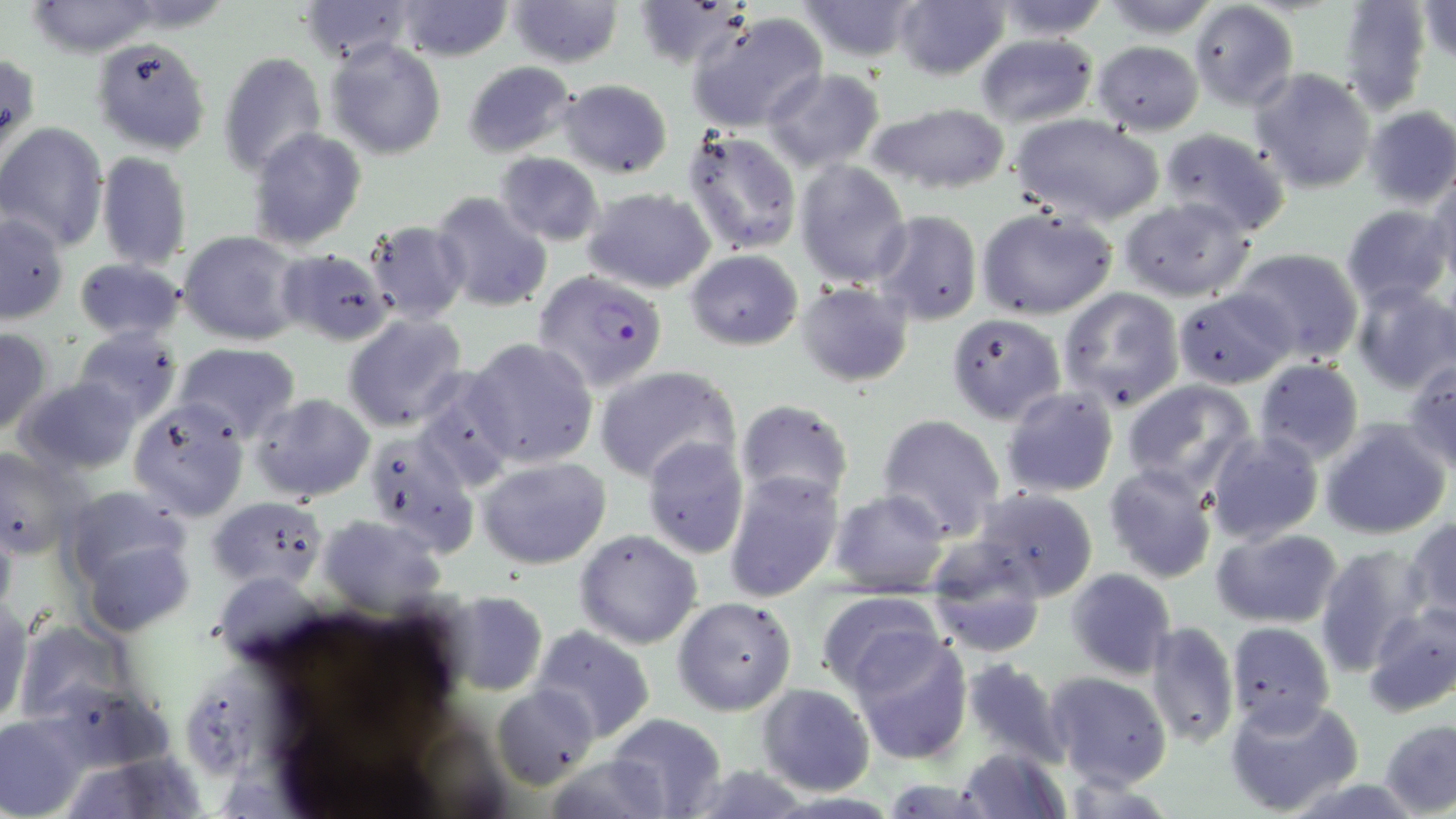
Approximate bounding boxes as [x1, y1, x2, y2] in pixels. Uninfected red blood cell locations: [22, 0, 169, 57], [396, 0, 513, 61], [507, 0, 625, 68], [792, 0, 925, 62], [893, 0, 1010, 81], [984, 0, 1113, 39], [1096, 0, 1224, 37], [1418, 0, 1455, 64], [295, 1, 419, 65], [1337, 1, 1433, 114], [1190, 2, 1298, 113], [686, 13, 827, 134], [975, 34, 1097, 126], [90, 36, 212, 156], [323, 38, 448, 160], [1092, 40, 1204, 133], [217, 51, 327, 176], [461, 60, 579, 159], [761, 68, 886, 172], [1250, 69, 1378, 194], [555, 79, 674, 179], [861, 103, 1012, 197], [1364, 105, 1456, 210], [1008, 114, 1166, 226], [0, 122, 108, 249], [247, 128, 368, 250], [682, 128, 801, 256], [1159, 128, 1291, 238], [95, 151, 193, 270], [494, 151, 606, 246], [794, 160, 911, 287], [1427, 174, 1456, 288], [581, 186, 715, 293], [430, 192, 554, 313], [1118, 197, 1257, 302], [1340, 205, 1451, 309], [975, 206, 1120, 320], [871, 209, 982, 325], [0, 215, 69, 324], [363, 217, 470, 323], [178, 230, 304, 344], [1230, 247, 1364, 362], [278, 248, 395, 345], [685, 250, 803, 349], [73, 257, 185, 343], [1349, 281, 1456, 395], [794, 282, 915, 386], [1057, 287, 1183, 412], [1173, 289, 1296, 388], [342, 313, 470, 432], [947, 313, 1066, 424], [72, 326, 182, 425], [0, 328, 50, 436], [466, 338, 598, 468], [175, 343, 300, 442], [1404, 358, 1456, 472], [1253, 360, 1366, 467], [594, 365, 739, 485], [411, 372, 521, 493], [13, 375, 142, 478], [1121, 379, 1258, 497], [1001, 386, 1120, 498], [249, 392, 375, 502], [127, 398, 251, 521], [733, 398, 855, 508], [876, 413, 1007, 541], [1320, 419, 1452, 539], [363, 431, 479, 558], [1204, 432, 1324, 544], [642, 437, 752, 560], [1, 446, 86, 560], [476, 456, 610, 570], [1103, 465, 1218, 585], [724, 472, 844, 602], [828, 488, 953, 597], [971, 489, 1101, 603], [209, 493, 328, 590], [65, 501, 196, 634], [317, 514, 448, 615], [1404, 516, 1456, 626], [1212, 527, 1344, 629], [574, 529, 703, 649], [924, 544, 1051, 657], [1313, 545, 1428, 674], [1065, 567, 1177, 680], [437, 590, 549, 695], [816, 591, 946, 698], [672, 596, 797, 715], [0, 599, 32, 728], [1362, 601, 1456, 718], [16, 619, 140, 726], [1143, 619, 1238, 752], [1225, 620, 1336, 735], [530, 626, 655, 745], [849, 631, 972, 763], [958, 657, 1070, 769], [1044, 671, 1175, 791], [757, 683, 875, 795], [492, 686, 597, 790], [1226, 695, 1364, 817], [607, 711, 725, 816], [0, 714, 90, 818], [1379, 719, 1456, 816], [957, 747, 1069, 818], [541, 754, 671, 819]. Plasmodium falciparum-infected red blood cell locations: [532, 270, 669, 393]. Slide-level diagnosis: Plasmodium falciparum. May-Grünwald-Giemsa stain. Thin blood film. 1000x magnification. Optical microscopy. Image is 1456×819 pixels. One field of a larger specimen.